State which parasite is depicted.
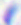

Toxoplasma gondii.

Summary:
  - Modality: photomicrograph
  - Magnification: 400x